State the blood parasite species.
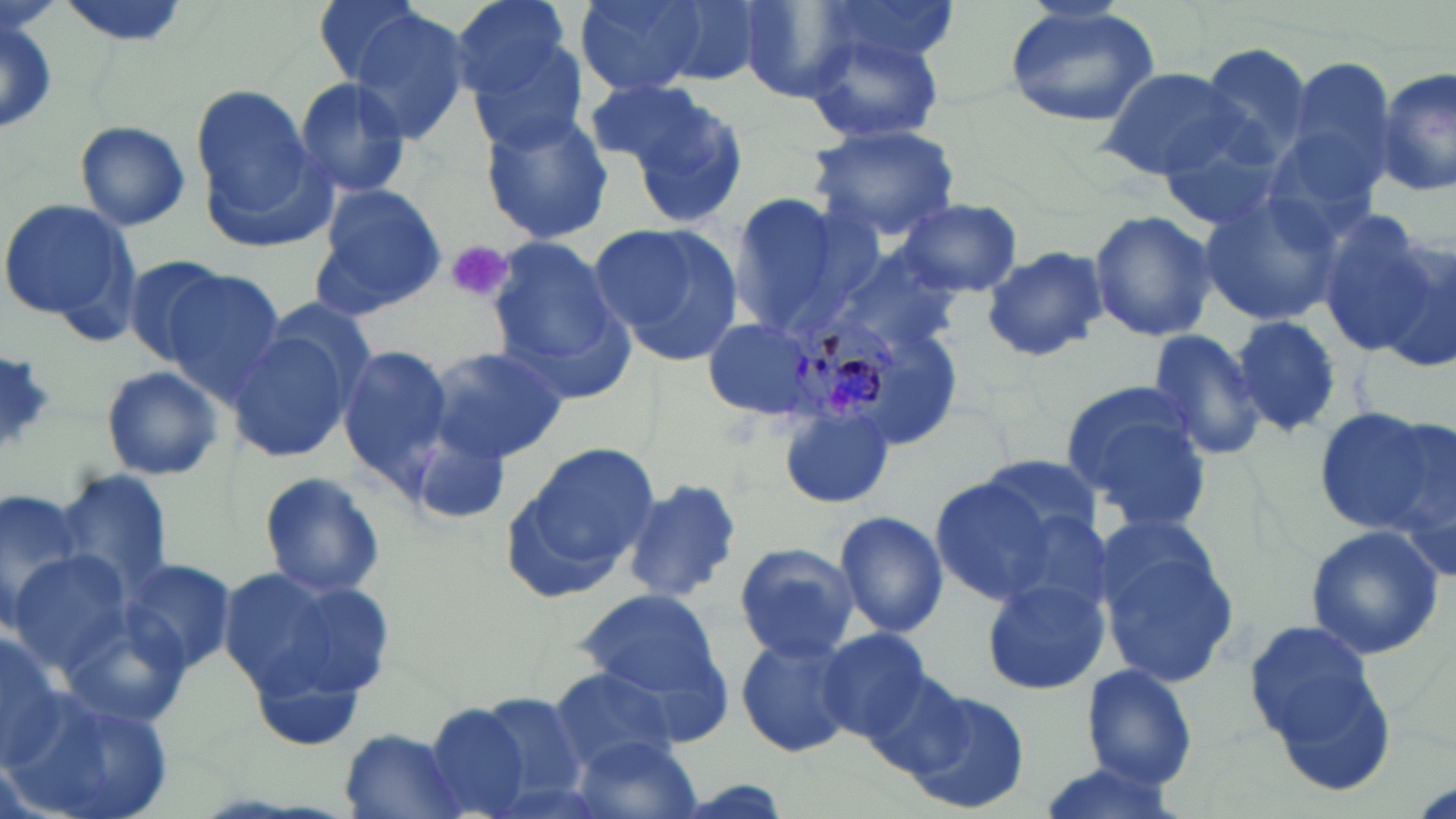
Plasmodium malariae.

Approximate bounding boxes as named x1/y1/x2/y2 corners in pixels. Platelet locations: (x1=446, y1=243, x2=511, y2=303). Plasmodium malariae-infected red blood cell locations: (x1=790, y1=311, x2=903, y2=430). Uninfected red blood cell locations: (x1=311, y1=0, x2=430, y2=90), (x1=450, y1=0, x2=578, y2=106), (x1=574, y1=0, x2=711, y2=93), (x1=646, y1=0, x2=774, y2=85), (x1=733, y1=0, x2=865, y2=101), (x1=810, y1=0, x2=958, y2=72), (x1=1003, y1=3, x2=1163, y2=129), (x1=344, y1=9, x2=476, y2=145), (x1=0, y1=13, x2=58, y2=140), (x1=804, y1=29, x2=946, y2=146), (x1=464, y1=33, x2=591, y2=153), (x1=1197, y1=44, x2=1315, y2=168), (x1=1281, y1=58, x2=1397, y2=195), (x1=1377, y1=65, x2=1454, y2=199), (x1=1098, y1=67, x2=1247, y2=180), (x1=582, y1=76, x2=726, y2=177), (x1=294, y1=77, x2=412, y2=200), (x1=190, y1=83, x2=326, y2=243), (x1=619, y1=85, x2=751, y2=230), (x1=1258, y1=107, x2=1392, y2=243), (x1=479, y1=110, x2=616, y2=244), (x1=1153, y1=116, x2=1295, y2=235), (x1=75, y1=121, x2=190, y2=232), (x1=805, y1=122, x2=959, y2=243), (x1=312, y1=187, x2=445, y2=316), (x1=722, y1=188, x2=867, y2=337), (x1=1197, y1=189, x2=1345, y2=326), (x1=899, y1=197, x2=1022, y2=296), (x1=0, y1=198, x2=138, y2=332), (x1=1088, y1=208, x2=1216, y2=346), (x1=1313, y1=211, x2=1444, y2=357), (x1=590, y1=222, x2=744, y2=361), (x1=483, y1=236, x2=631, y2=396), (x1=981, y1=245, x2=1109, y2=362), (x1=825, y1=247, x2=966, y2=364), (x1=120, y1=255, x2=233, y2=364), (x1=159, y1=268, x2=287, y2=398), (x1=223, y1=314, x2=369, y2=467), (x1=1233, y1=315, x2=1342, y2=434), (x1=701, y1=316, x2=825, y2=422), (x1=1145, y1=327, x2=1267, y2=462), (x1=428, y1=347, x2=569, y2=464), (x1=336, y1=348, x2=451, y2=484), (x1=0, y1=353, x2=57, y2=452), (x1=99, y1=365, x2=225, y2=482), (x1=1059, y1=386, x2=1212, y2=530), (x1=776, y1=406, x2=895, y2=507), (x1=1316, y1=406, x2=1447, y2=536), (x1=410, y1=423, x2=515, y2=525), (x1=515, y1=440, x2=660, y2=578), (x1=980, y1=456, x2=1105, y2=543), (x1=59, y1=465, x2=175, y2=604), (x1=258, y1=470, x2=385, y2=599), (x1=928, y1=471, x2=1087, y2=606), (x1=621, y1=478, x2=743, y2=606), (x1=0, y1=486, x2=94, y2=633), (x1=834, y1=509, x2=949, y2=641), (x1=1094, y1=522, x2=1241, y2=692), (x1=1304, y1=524, x2=1443, y2=660), (x1=733, y1=544, x2=861, y2=663), (x1=6, y1=552, x2=135, y2=677), (x1=115, y1=557, x2=234, y2=679), (x1=219, y1=566, x2=395, y2=710), (x1=981, y1=577, x2=1109, y2=697), (x1=576, y1=590, x2=726, y2=697), (x1=1243, y1=616, x2=1392, y2=777), (x1=813, y1=626, x2=936, y2=745), (x1=0, y1=633, x2=65, y2=768), (x1=734, y1=633, x2=857, y2=758), (x1=1081, y1=663, x2=1199, y2=790), (x1=548, y1=666, x2=682, y2=772), (x1=3, y1=678, x2=181, y2=819), (x1=900, y1=686, x2=1031, y2=816), (x1=457, y1=689, x2=596, y2=816), (x1=426, y1=704, x2=537, y2=817), (x1=337, y1=730, x2=466, y2=818), (x1=572, y1=734, x2=704, y2=819), (x1=1030, y1=762, x2=1188, y2=819). Image is 1456×819 pixels. Thin blood film. Captured at 1000x magnification. Single field of view. May-Grünwald-Giemsa-stained preparation. Light microscopy.